State which cell type is depicted.
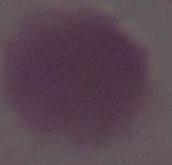

An erythrocyte.

Captured at 1000x magnification. Photomicrograph.